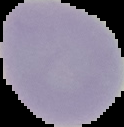
preparation = thin blood film
image size = 124×127 pixels
image type = segmented cell region on a black background
malaria status = uninfected